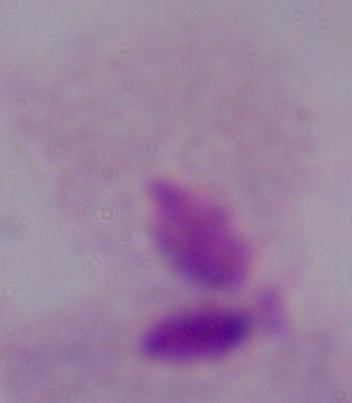
identification = trichomonad
modality = micrograph
magnification = 1000x